Identify the parasite.
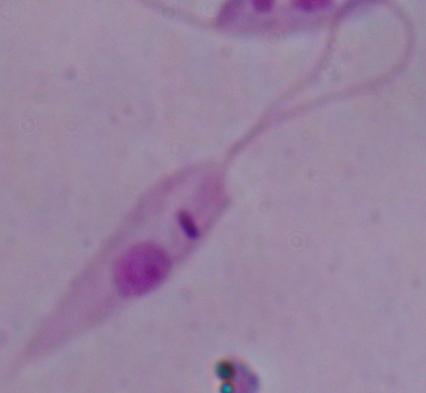

This is Leishmania.

1000x magnification. Micrograph.